Locate every leukocyte (white blood cell).
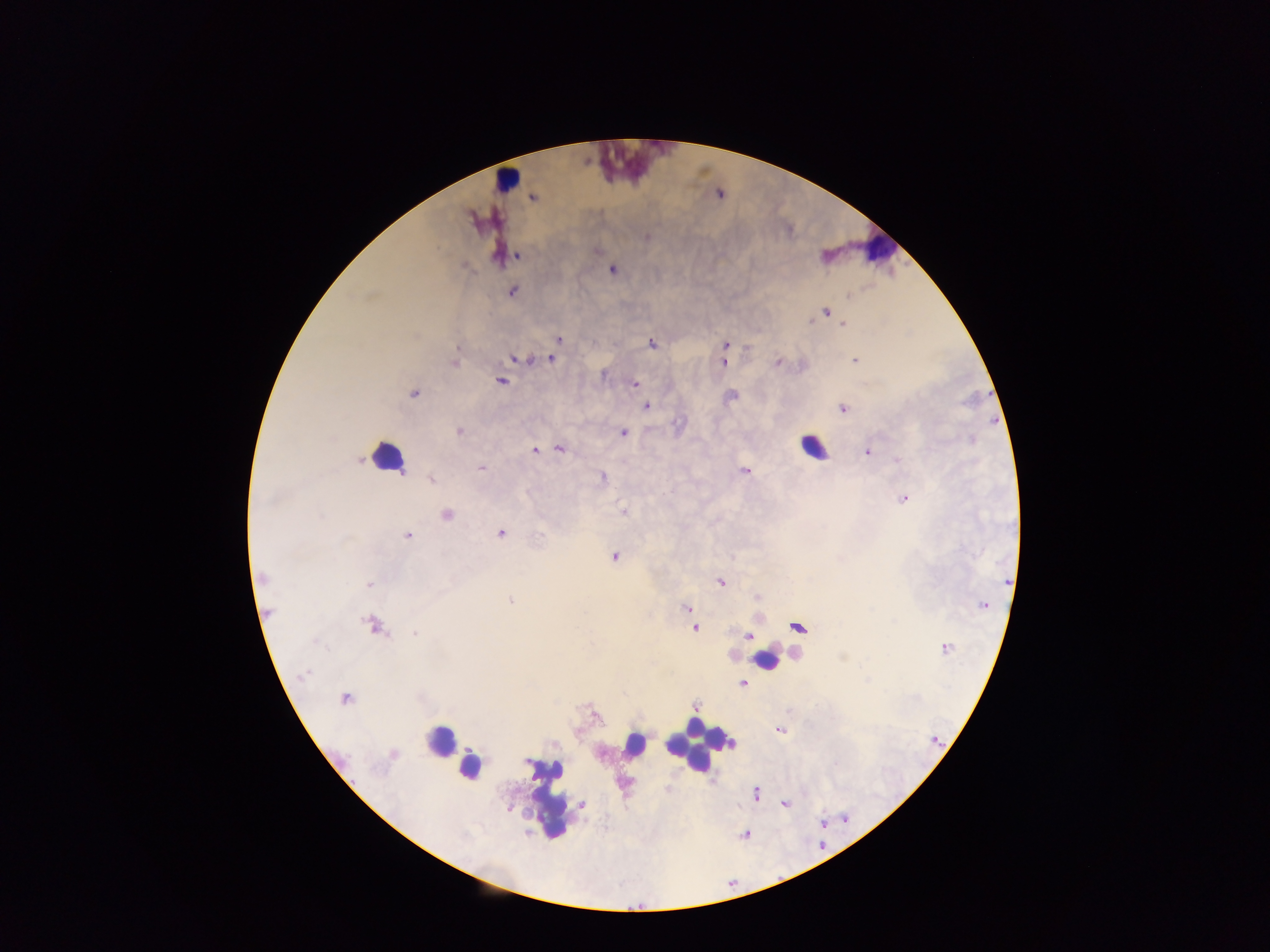

Approximate centers as {x, y} in pixels.
Leukocytes: {628, 165}, {507, 180}, {879, 248}, {813, 448}, {386, 457}, {766, 659}, {440, 741}, {635, 745}, {700, 745}, {469, 766}, {546, 798}.

Plasmodium parasite locations: {532, 197}, {518, 255}, {612, 269}, {512, 290}, {825, 310}, {843, 324}, {558, 339}, {652, 343}, {725, 345}, {513, 358}, {551, 358}, {854, 360}, {454, 361}, {723, 361}, {778, 362}, {500, 380}, {635, 383}, {413, 393}, {645, 407}, {843, 407}, {458, 432}, {623, 432}, {560, 448}, {534, 450}, {868, 451}, {480, 468}, {744, 470}, {602, 478}, {431, 479}, {902, 498}, {623, 511}, {446, 514}, {500, 533}, {407, 535}, {613, 557}, {263, 577}, {719, 581}, {369, 584}, {510, 600}, {983, 605}, {687, 608}, {266, 613}, {373, 625}, {796, 626}, {694, 628}, {749, 636}, {945, 647}, {743, 682}, {345, 698}, {694, 706}, {780, 729}, {756, 793}, {581, 804}, {784, 804}. Collected in Ghana. One field of view. Photographed through a microscope with a mobile-phone camera. Image is 1270×952 pixels. Thick blood smear.